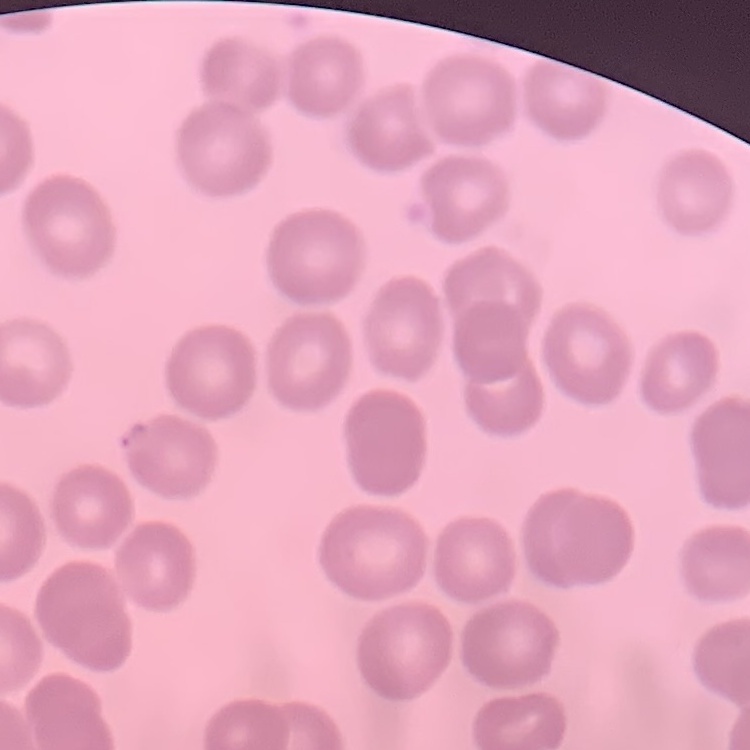
red blood cell morphology = no rouleaux formation
image type = square crop of a larger photomicrograph
preparation = thin blood smear
stain = Field's or Giemsa